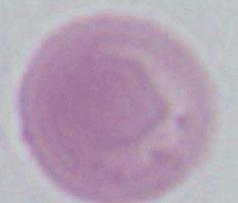

Photomicrograph. Captured at 1000x magnification. A red blood cell is shown.